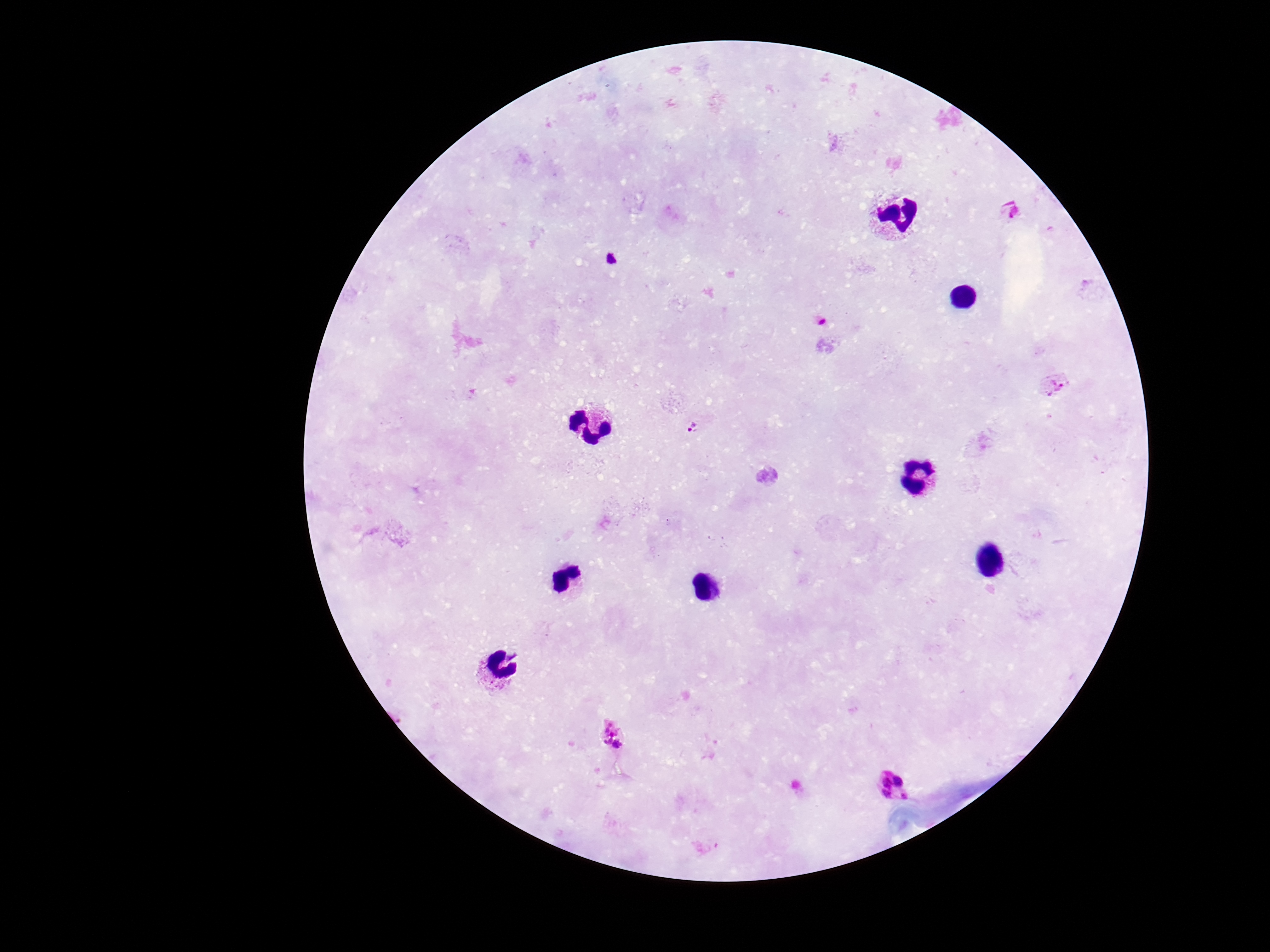

Approximate centers as (x, y) in pixels.
Summary:
  - Plasmodium parasite locations: (1014, 211), (1053, 384), (691, 427), (612, 734), (895, 789)
  - Preparation: thick peripheral-blood smear
  - Capture: smartphone camera through the microscope eyepiece
  - Field of view: single
  - Magnification: 100x
  - Patient malaria status: infected
  - Stain: Giemsa
  - Image size: 1270×952 pixels